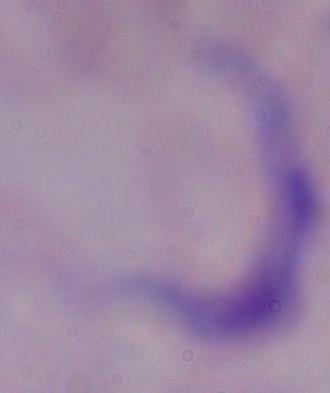 1000x magnification. Micrograph. A trypanosome is shown.